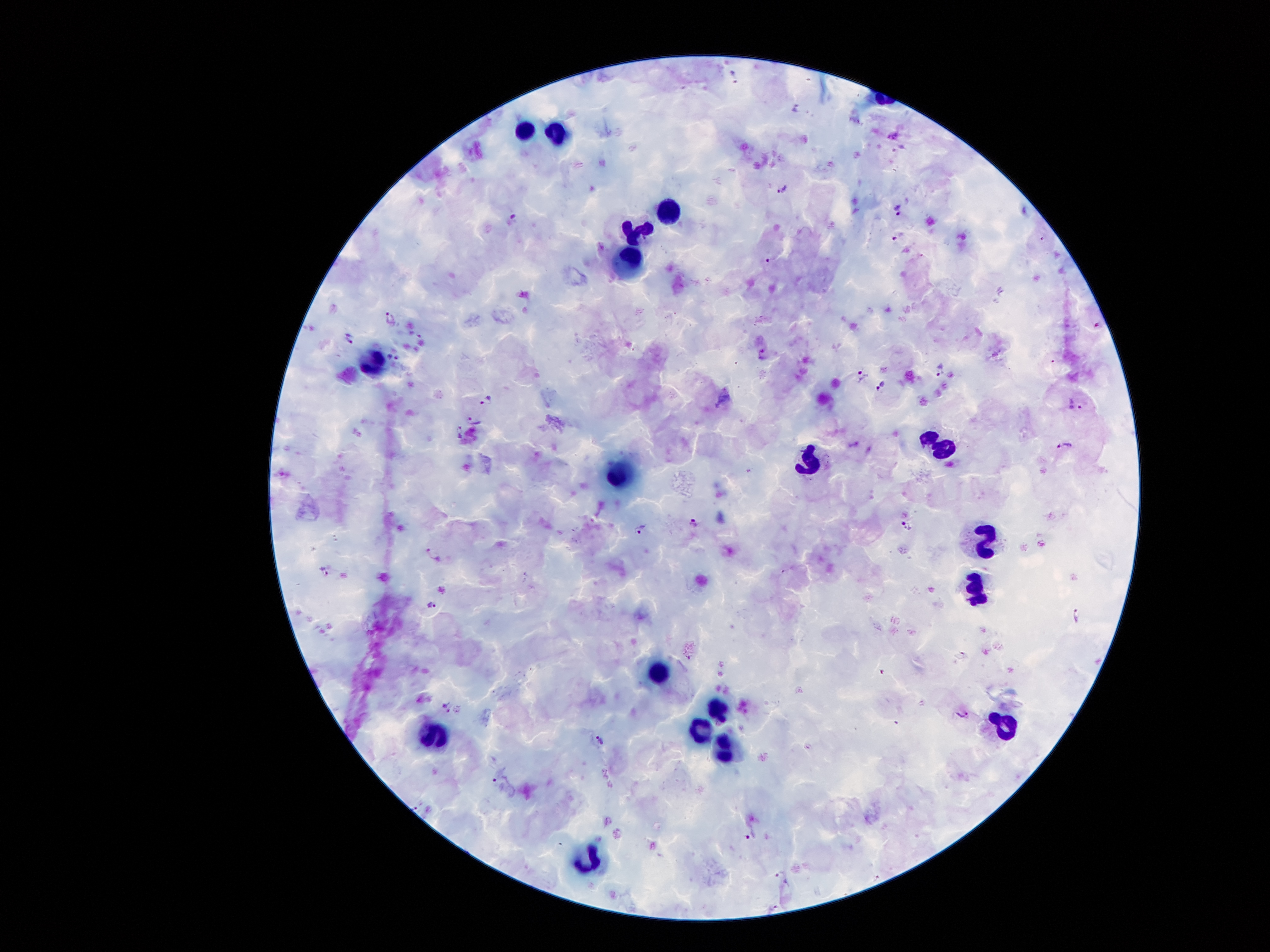 Approximate object centers, in pixels from the top-left corner. Plasmodium parasite locations: (x=783, y=190), (x=390, y=318), (x=350, y=339), (x=392, y=358), (x=882, y=387), (x=485, y=400), (x=473, y=421), (x=461, y=432), (x=694, y=522), (x=639, y=529), (x=326, y=573), (x=430, y=606), (x=1077, y=615), (x=599, y=739), (x=416, y=809), (x=781, y=874), (x=773, y=907). Leukocyte locations: (x=522, y=132), (x=558, y=133), (x=671, y=210), (x=638, y=232), (x=626, y=259), (x=375, y=362), (x=936, y=443), (x=813, y=462), (x=618, y=475), (x=985, y=539), (x=974, y=588), (x=657, y=672), (x=717, y=708), (x=1003, y=724), (x=699, y=727), (x=434, y=734), (x=726, y=755), (x=588, y=860). Giemsa stain. Single field of view. Smartphone photograph taken through the microscope eyepiece. Image is 1270×952 pixels. 100x magnification. Patient malaria status: infected with Plasmodium falciparum. Thick blood film.